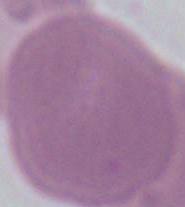

Photomicrograph. Captured at 1000x magnification. A red blood cell is shown.